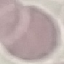

result = no malaria parasites seen
capture = smartphone camera at the microscope eyepiece
preparation = thin smear
image type = cell patch, automatically extracted from a larger field of view and resized to 64 × 64 pixels
stain = Giemsa